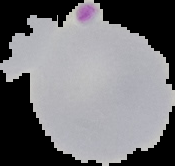

Image is 175×166 pixels. The area outside the segmented cell region is set to black. Result: Plasmodium parasites detected. From a thin blood smear.